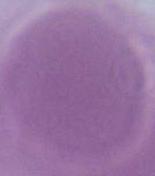
Summary:
  - Magnification: 1000x
  - Modality: micrograph
  - Identification: red blood cell